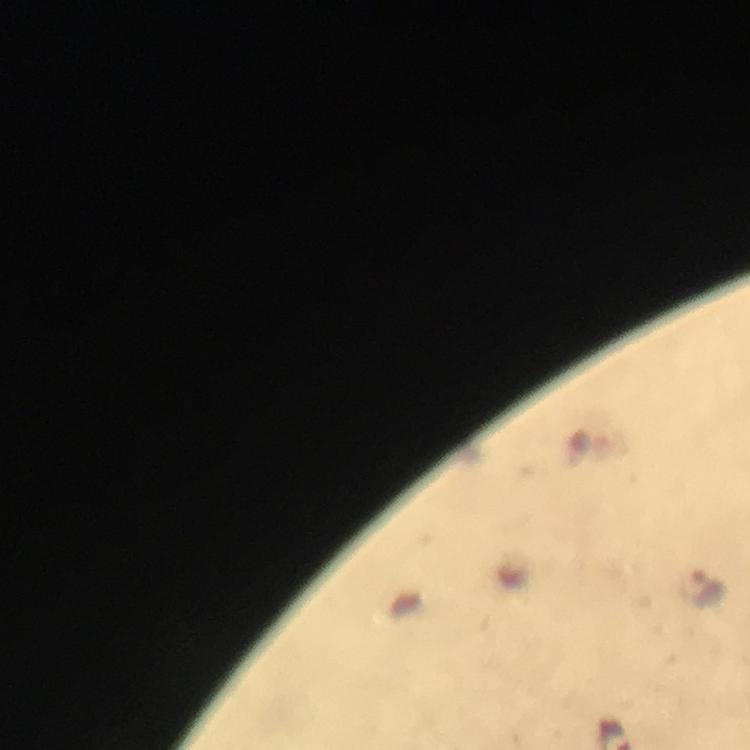
Approximate centers as (x, y) in pixels. Plasmodium parasite locations: (702, 586). Thick blood smear. 100x magnification. From a diagnostic examination for malaria. Immersion oil was used. Giemsa stain. Smartphone photograph taken through a microscope. A crop from one field of view. Image is 750×750 pixels.